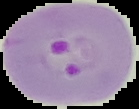

The area outside the segmented cell region is set to black. From a thin blood smear. Image is 139×109 pixels. Malaria status: parasitized.